Evaluate for malaria.
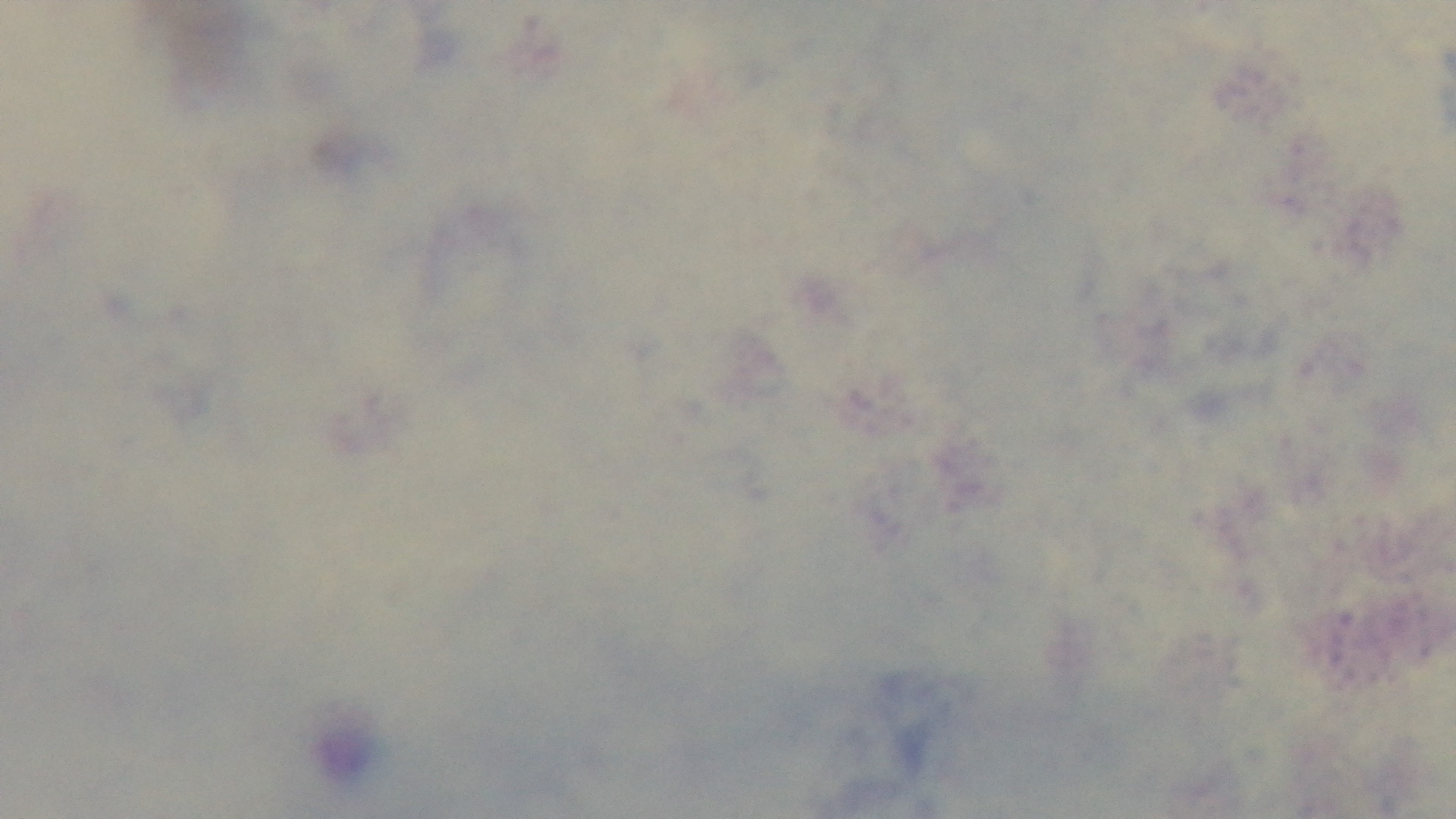
Uninfected.

Summary:
  - Stain: Giemsa
  - Field of view: one from the slide
  - Objective: 100x oil immersion
  - Capture: mounted 4K digital camera
  - Preparation: thick
  - Modality: light microscopy